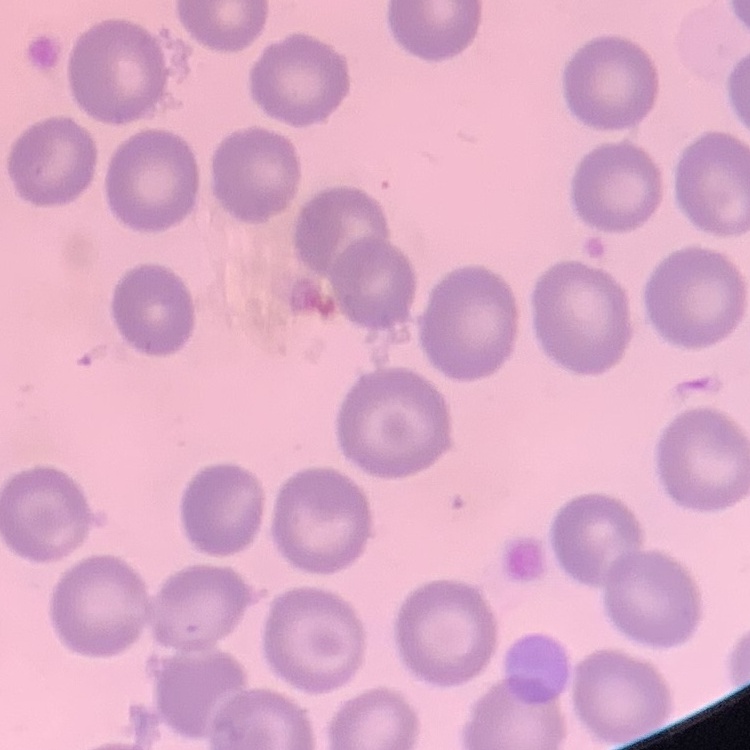

{
  "red_blood_cell_morphology": "no rouleaux formation",
  "image_type": "square crop of a larger photomicrograph",
  "stain": "Field's or Giemsa",
  "preparation": "thin blood smear"
}